Outline each blood parasite and name the species.
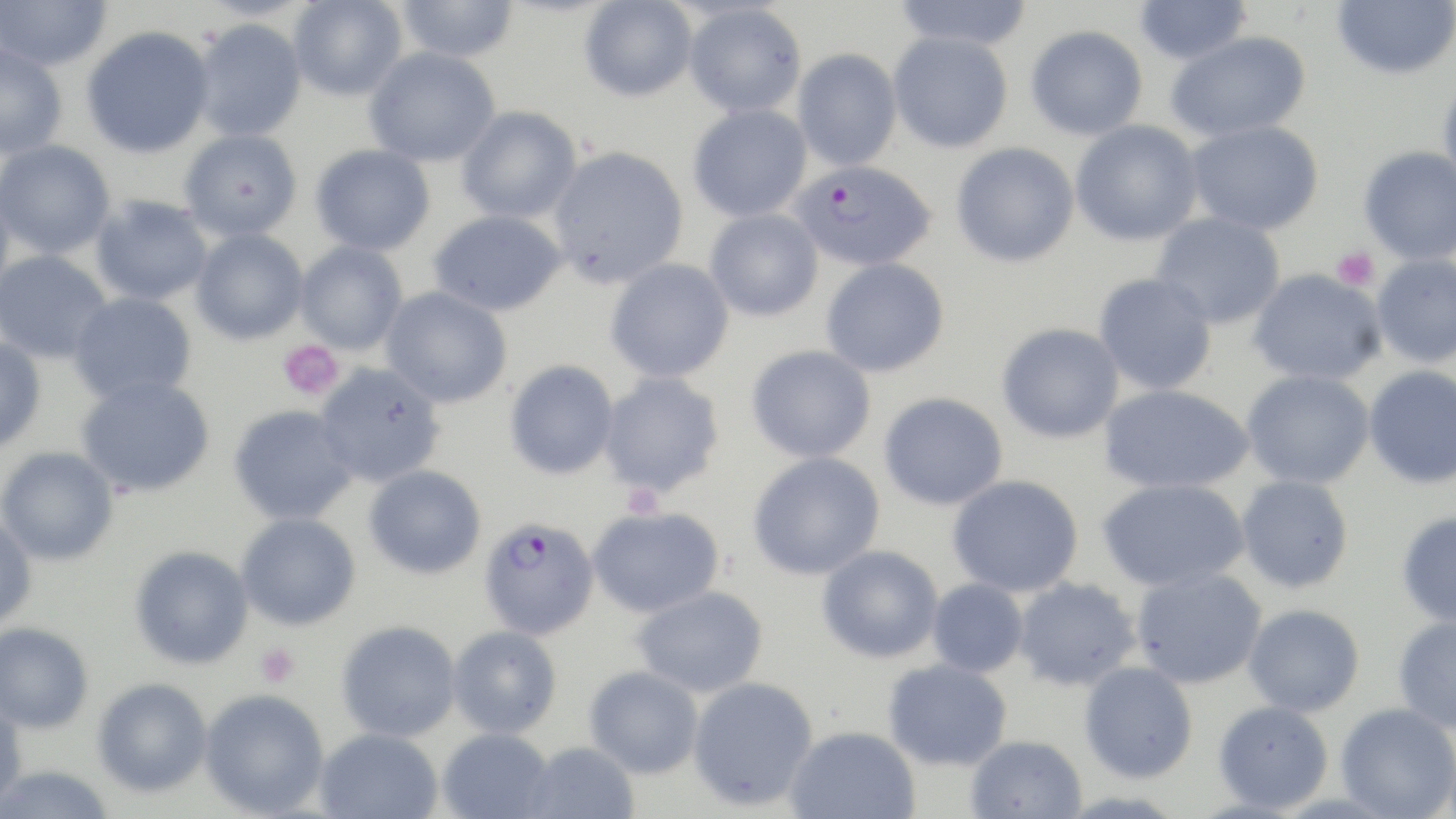
Approximate bounding boxes as (x1,y1)-(x2,y2) corner pairs in pixels.
Plasmodium falciparum-infected red blood cells: (790,162)-(937,268), (478,518)-(600,641).
No Plasmodium ovale, Plasmodium malariae, Plasmodium vivax, Babesia divergens, or Trypanosoma brucei observed.

slide_level_diagnosis: Plasmodium falciparum
preparation: thin blood smear
magnification: 1000x
field_of_view: single
stain: May-Grünwald-Giemsa
platelet_locations: 'approximate bounding boxes as (x1,y1)-(x2,y2) corner pairs in pixels: (1331,246)-(1380,292), (278,339)-(345,400), (622,484)-(664,521), (255,642)-(300,687)'
uninfected_red_blood_cell_locations: 'approximate bounding boxes as (x1,y1)-(x2,y2) corner pairs in pixels: (0,0)-(113,72), (289,0)-(407,101), (395,0)-(519,62), (579,0)-(697,101), (892,0)-(1034,51), (1134,0)-(1252,66), (1332,0)-(1455,79), (683,3)-(806,117), (191,19)-(307,142), (1025,25)-(1148,141), (81,26)-(214,158), (888,31)-(1013,153), (1165,31)-(1311,142), (0,44)-(68,160), (364,47)-(500,167), (793,48)-(902,170), (1438,74)-(1456,192), (688,104)-(812,222), (456,106)-(581,223), (1071,120)-(1202,246), (1186,120)-(1324,235), (179,129)-(302,242), (0,140)-(115,257), (951,142)-(1079,268), (310,144)-(435,256), (548,146)-(688,289), (1358,146)-(1456,264), (0,183)-(15,302), (90,195)-(212,305), (428,209)-(567,317), (704,209)-(823,322), (1151,212)-(1285,329), (191,229)-(308,345), (295,241)-(408,354), (0,250)-(112,363), (1371,254)-(1456,367), (821,258)-(950,378), (605,259)-(734,383), (1248,269)-(1386,385), (1093,273)-(1217,394), (381,286)-(512,408), (68,291)-(197,406), (996,323)-(1124,443), (0,336)-(47,454), (746,346)-(876,463), (504,360)-(618,480), (315,363)-(445,487), (1364,365)-(1456,489), (1242,370)-(1374,489), (598,372)-(725,498), (76,377)-(214,497), (1098,384)-(1253,494), (878,392)-(1008,510), (228,405)-(358,525), (0,447)-(119,566), (748,452)-(885,580), (363,464)-(486,579), (947,474)-(1083,597), (1236,474)-(1354,593), (1097,477)-(1250,593), (587,507)-(724,618), (1396,511)-(1456,627), (236,513)-(361,630), (0,515)-(37,630), (129,545)-(254,670), (817,545)-(943,663), (1130,567)-(1267,689), (1012,577)-(1141,691), (927,578)-(1028,677), (631,586)-(768,697), (1243,603)-(1365,716), (1392,615)-(1456,733), (336,620)-(461,742), (0,622)-(94,734), (448,626)-(562,739), (882,658)-(1012,770), (1079,661)-(1198,783), (584,666)-(703,779), (687,676)-(819,811), (93,678)-(212,798), (199,689)-(329,817), (0,699)-(27,811), (1213,700)-(1334,813), (1336,703)-(1456,819), (784,725)-(921,819), (314,727)-(443,818), (437,728)-(554,819), (965,735)-(1087,819), (523,742)-(640,819), (0,765)-(117,819)'
image_size: 1456×819 pixels
modality: optical microscopy